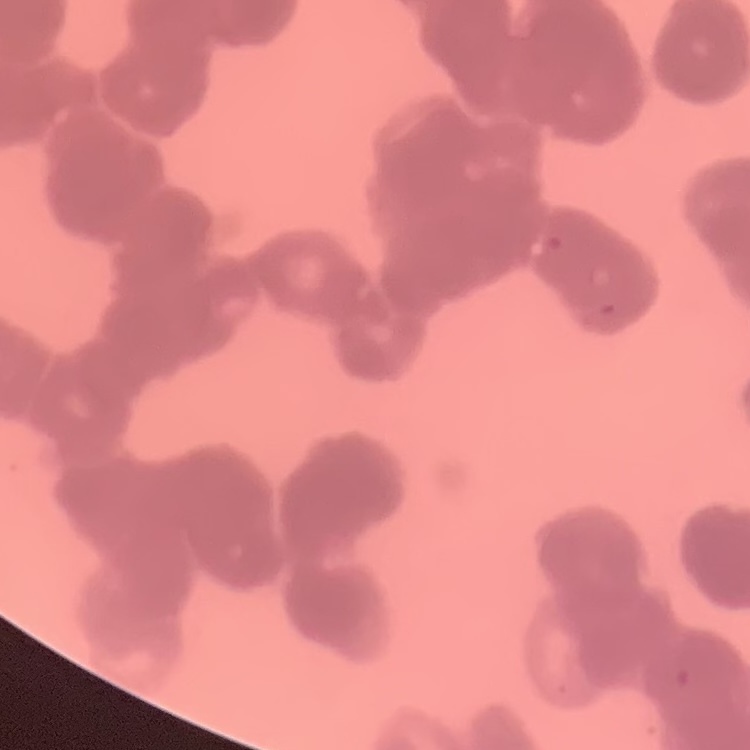
erythrocyte morphology = rouleaux formation
stain = Field's or Giemsa
preparation = thin blood smear
image type = one tile cut from a larger photomicrograph